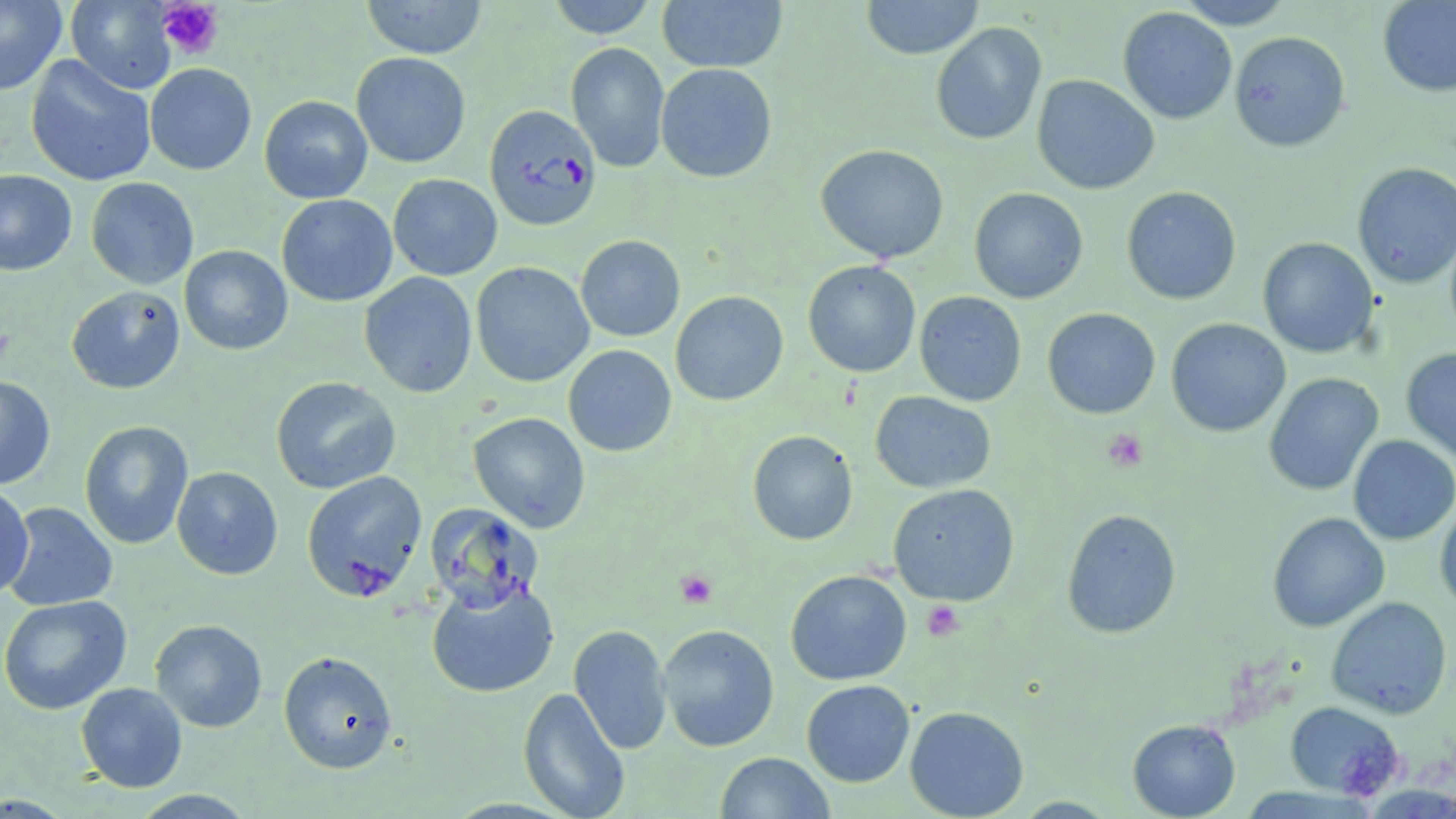 Approximate bounding boxes as (x1, y1, x2, y2) in pixels. Uninfected red blood cell locations: (545, 0, 659, 38), (860, 0, 984, 59), (1175, 0, 1295, 29), (0, 1, 67, 96), (65, 1, 178, 94), (360, 1, 489, 59), (656, 1, 788, 73), (1377, 1, 1456, 97), (1118, 7, 1237, 124), (930, 22, 1047, 146), (1229, 31, 1350, 152), (566, 42, 670, 173), (351, 52, 471, 168), (25, 55, 156, 187), (145, 63, 257, 175), (655, 63, 778, 183), (1032, 75, 1159, 195), (259, 95, 373, 204), (815, 144, 949, 263), (1351, 162, 1456, 289), (0, 170, 77, 276), (388, 174, 502, 280), (85, 177, 199, 289), (1122, 186, 1242, 305), (969, 187, 1088, 304), (277, 194, 398, 307), (575, 235, 685, 342), (1257, 237, 1379, 358), (179, 245, 292, 355), (802, 260, 921, 378), (470, 261, 595, 388), (359, 272, 477, 398), (66, 286, 185, 394), (670, 291, 788, 406), (914, 291, 1027, 406), (1042, 308, 1160, 419), (1165, 318, 1291, 437), (563, 345, 677, 457), (1401, 347, 1456, 464), (1263, 372, 1383, 496), (0, 375, 56, 490), (270, 376, 401, 494), (870, 391, 996, 493), (468, 412, 590, 533), (79, 420, 194, 549), (747, 430, 858, 545), (1348, 435, 1456, 545), (171, 466, 283, 580), (301, 470, 427, 602), (888, 483, 1020, 606), (0, 484, 34, 601), (1435, 499, 1456, 614), (4, 502, 118, 611), (424, 503, 544, 613), (1061, 508, 1181, 639), (1267, 512, 1390, 633), (785, 570, 912, 686), (426, 579, 559, 699), (0, 595, 132, 715), (1326, 596, 1453, 720), (150, 619, 268, 733), (657, 624, 779, 751), (569, 625, 673, 754), (278, 651, 398, 774), (802, 680, 915, 787), (75, 682, 187, 792), (517, 687, 631, 819), (1284, 701, 1404, 800), (905, 706, 1029, 818), (1127, 718, 1240, 818), (716, 752, 836, 818), (128, 789, 260, 818), (1013, 797, 1118, 818). Plasmodium falciparum-infected red blood cell locations: (484, 104, 601, 231). Platelet locations: (157, 0, 223, 60), (0, 326, 14, 367), (1102, 428, 1148, 472), (675, 569, 717, 608), (922, 600, 964, 641). Slide-level diagnosis: Plasmodium falciparum. May-Grünwald-Giemsa stain. Captured at 1000x magnification. Single field of view. Optical microscopy. Thin blood smear. Image is 1456×819 pixels.